Describe the morphology of the red blood cells.
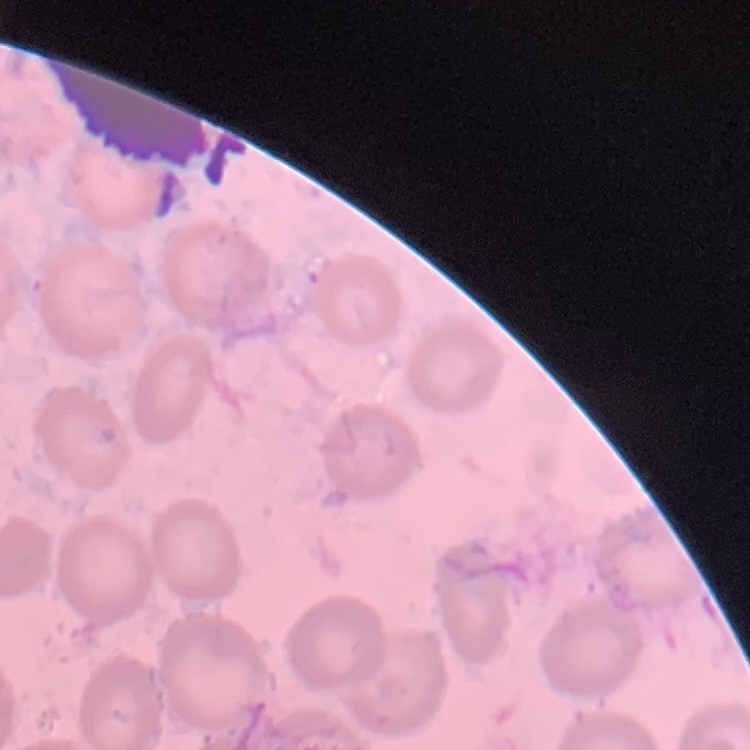

They show no rouleaux formation.

Summary:
  - Stain: Field's or Giemsa
  - Image type: one tile cut from a larger photomicrograph
  - Preparation: thin blood film